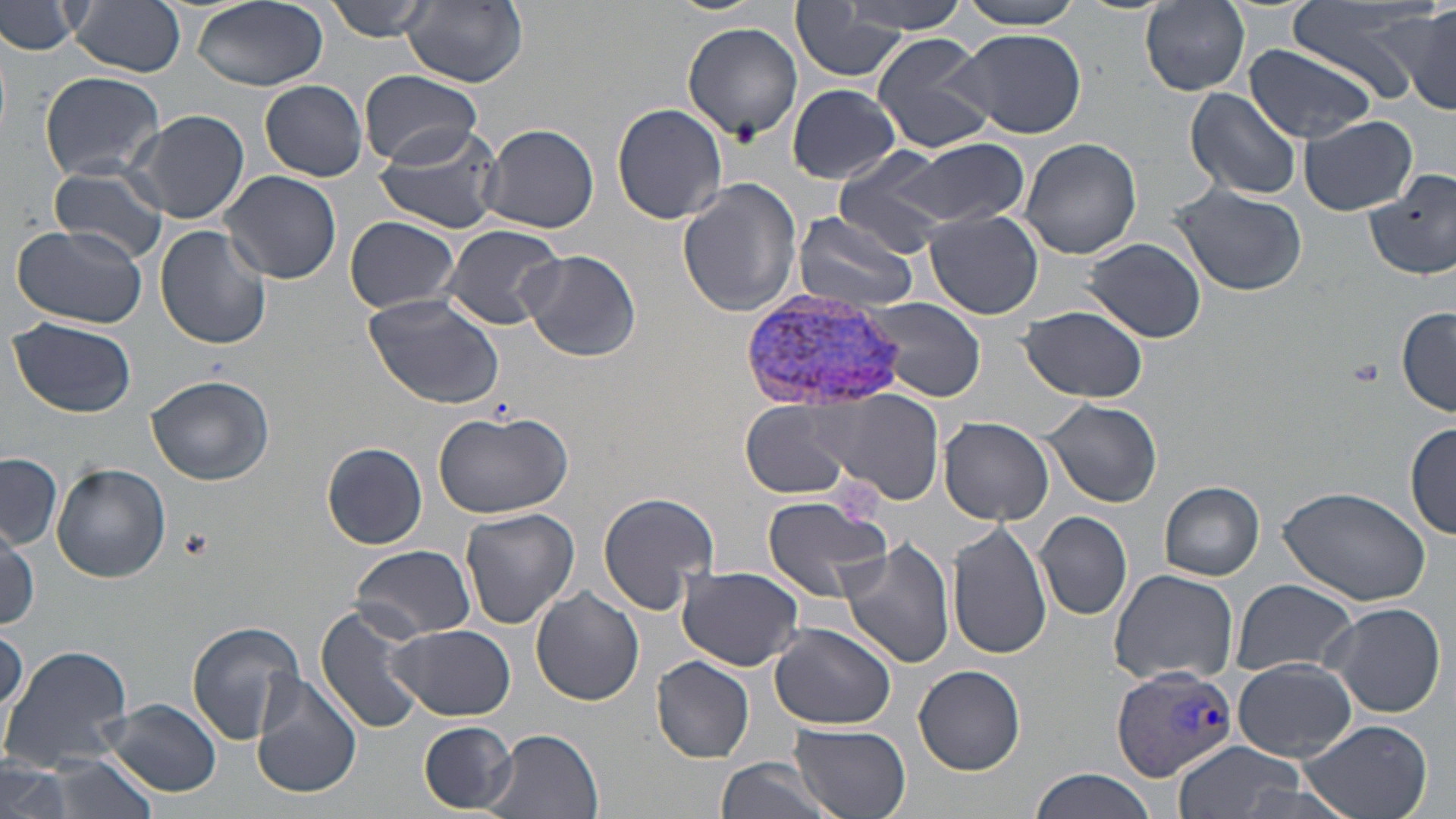

Approximate bounding boxes as (x1,y1)-(x2,y2) corner pairs in pixels. Platelet locations: (179,526)-(214,560). Uninfected red blood cell locations: (70,0)-(187,75), (190,0)-(328,92), (324,0)-(437,42), (663,0)-(771,16), (954,0)-(1088,30), (1288,0)-(1438,97), (0,1)-(90,56), (836,1)-(968,35), (1138,1)-(1252,97), (401,2)-(529,86), (788,4)-(914,84), (1399,8)-(1456,115), (683,21)-(803,140), (950,28)-(1091,140), (869,33)-(997,154), (1245,44)-(1379,143), (39,70)-(166,182), (360,70)-(483,167), (261,78)-(369,180), (786,83)-(902,184), (1185,87)-(1302,201), (611,103)-(728,225), (129,108)-(251,225), (1300,115)-(1418,215), (373,123)-(505,236), (481,123)-(598,236), (1019,137)-(1143,260), (903,140)-(1028,227), (831,153)-(956,258), (49,164)-(169,264), (1365,168)-(1456,281), (220,171)-(343,284), (677,178)-(804,317), (1169,183)-(1308,297), (925,209)-(1043,318), (790,211)-(921,311), (343,215)-(462,314), (438,221)-(565,332), (12,224)-(147,331), (154,224)-(273,351), (1084,237)-(1207,343), (520,248)-(642,361), (364,295)-(506,410), (859,295)-(989,403), (1020,305)-(1148,403), (1395,307)-(1456,416), (7,318)-(137,418), (145,374)-(276,487), (827,389)-(944,503), (1041,398)-(1162,508), (741,402)-(854,498), (431,406)-(576,518), (938,416)-(1055,525), (1406,421)-(1456,541), (321,441)-(426,548), (1,454)-(63,548), (52,462)-(170,582), (1158,480)-(1264,581), (1278,481)-(1433,607), (596,492)-(720,615), (759,493)-(890,601), (459,507)-(581,629), (1036,511)-(1133,620), (948,520)-(1051,659), (2,524)-(41,628), (837,538)-(955,670), (350,545)-(477,639), (677,565)-(805,671), (1107,570)-(1240,685), (1230,580)-(1360,678), (530,587)-(644,706), (1321,601)-(1447,718), (317,603)-(430,738), (186,621)-(305,744), (768,622)-(897,729), (389,624)-(516,721), (1,627)-(28,720), (0,645)-(134,774), (651,656)-(754,762), (1233,659)-(1357,760), (914,664)-(1025,774), (251,674)-(364,800), (102,698)-(222,796), (1299,719)-(1434,819), (419,722)-(517,812), (790,723)-(912,819), (483,729)-(605,819), (1171,740)-(1308,819), (32,754)-(163,819), (714,758)-(834,819), (2,760)-(73,819), (1030,768)-(1163,819). Plasmodium vivax-infected red blood cell locations: (741,291)-(911,409), (1112,665)-(1240,782). Slide-level diagnosis: Plasmodium vivax. Optical microscopy. One field of a larger specimen. May-Grünwald-Giemsa-stained preparation. Image is 1456×819 pixels. Thin blood smear. 1000x magnification.